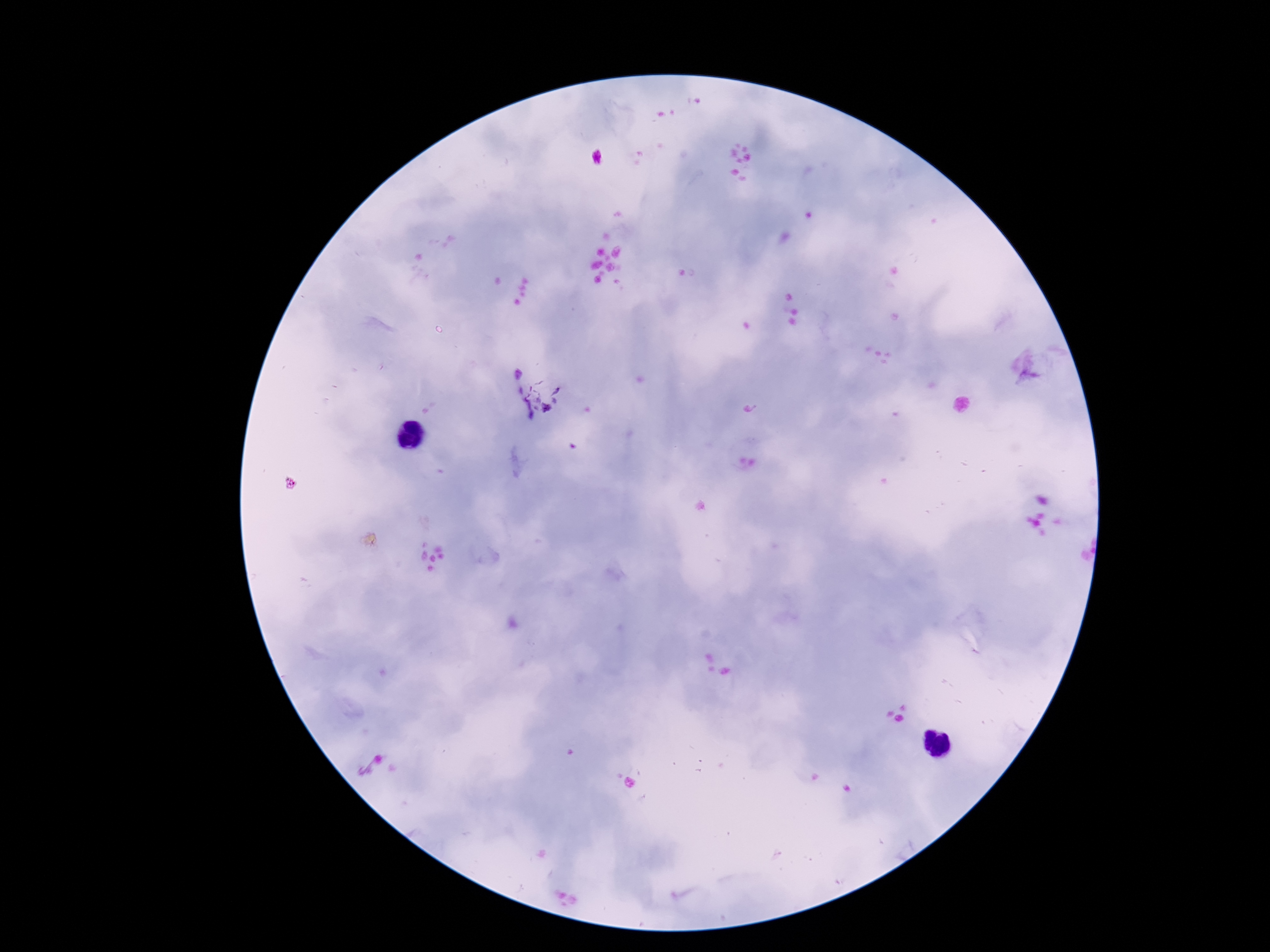
Approximate object centers, in pixels from the top-left corner. Plasmodium parasite locations: (x=546, y=392). Patient malaria status: infected. Giemsa stain. Thick peripheral-blood smear. Smartphone photograph taken through the microscope eyepiece. 100x magnification. Image is 1270×952 pixels. One field from this slide.